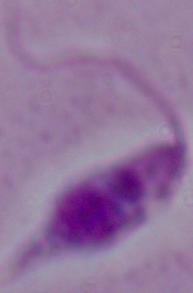 A Leishmania parasite is shown. Captured at 1000x magnification. Photomicrograph.